Assess this cell for malaria.
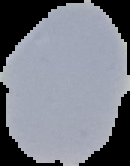

It is uninfected.

image type = cell region segmented out of the field of view; surrounding area masked to black
preparation = thin blood smear
image size = 130×166 pixels